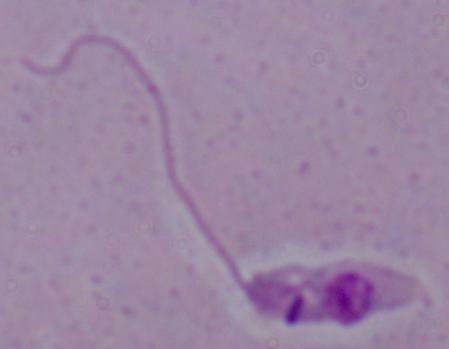
modality = photomicrograph
magnification = 1000x
identification = Leishmania